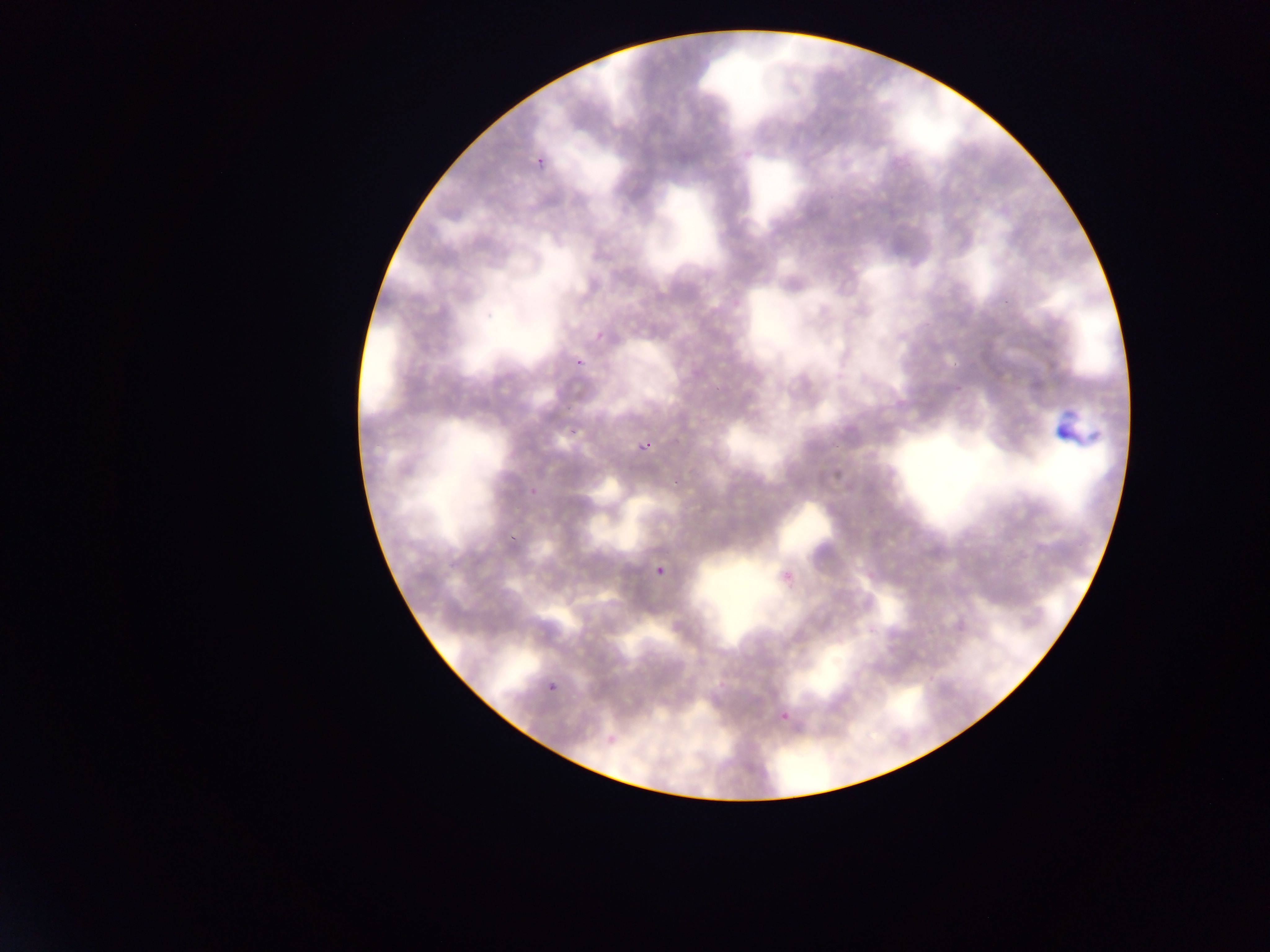

capture: mobile-phone photograph through a microscope
plasmodium_parasite_locations: 'approximate bounding boxes as [left, top, right, bottom] in pixels: [533, 149, 549, 174], [566, 350, 586, 367], [561, 411, 592, 443], [637, 440, 653, 453], [526, 485, 536, 500], [512, 519, 528, 539], [653, 557, 670, 577], [777, 561, 805, 584], [548, 682, 558, 692], [783, 703, 793, 720]'
country: Ghana
leukocyte_locations: 'approximate bounding boxes as [left, top, right, bottom] in pixels: [1039, 398, 1109, 454]'
field_of_view: single
preparation: thin blood smear
image_size: 1270×952 pixels